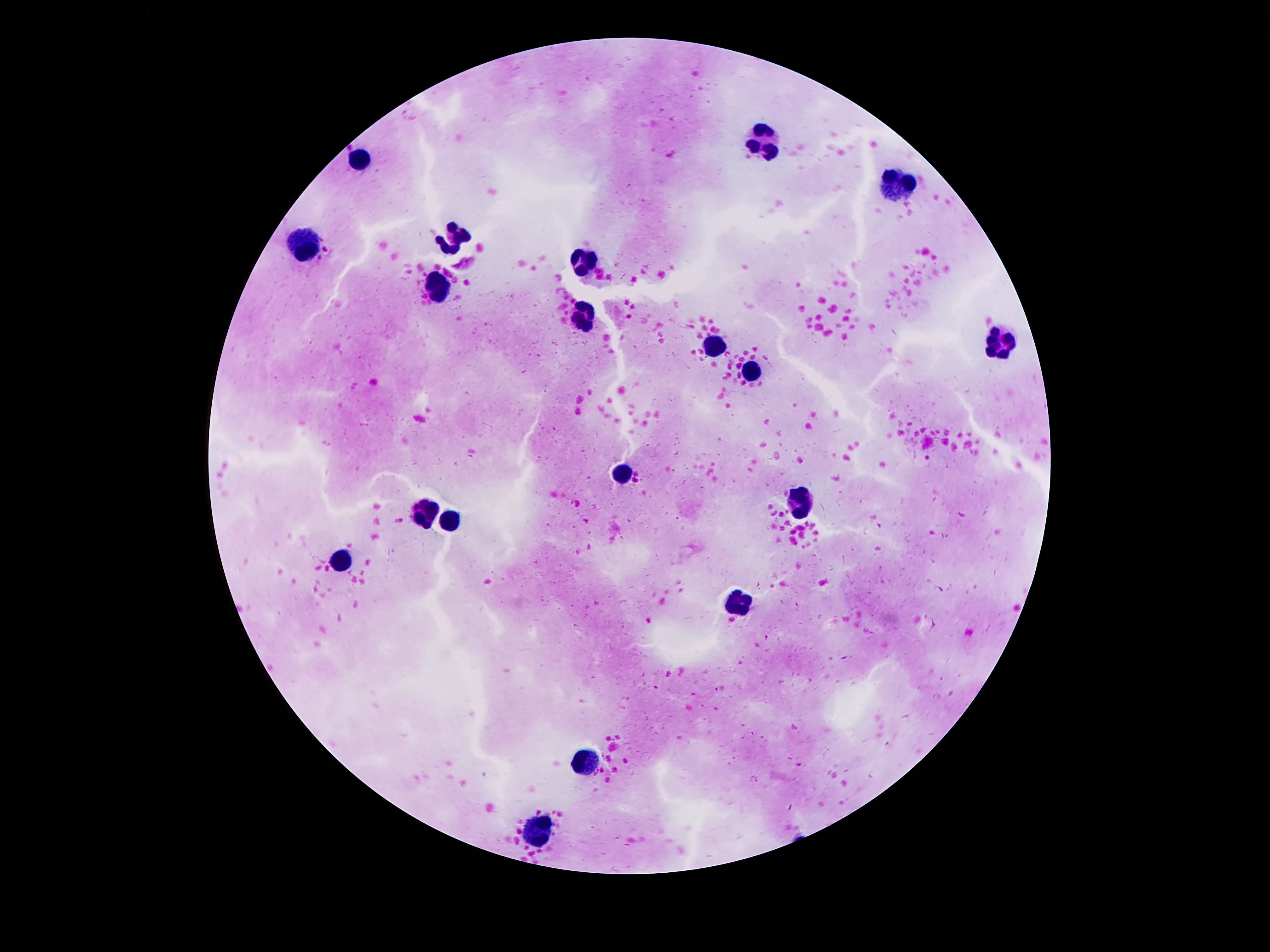

{
  "preparation": "thick blood smear",
  "image_size": "1270×952 pixels",
  "magnification": "100x",
  "patient_malaria_status": "uninfected",
  "capture": "smartphone camera through the microscope eyepiece",
  "field_of_view": "one from this slide",
  "leukocyte_locations": "approximate centers as [x, y] in pixels: [766, 141], [360, 159], [901, 186], [454, 235], [307, 243], [586, 261], [440, 285], [584, 317], [1002, 344], [715, 346], [752, 372], [625, 475], [803, 505], [424, 512], [448, 521], [344, 562], [741, 606], [590, 760], [543, 826]",
  "stain": "Giemsa"
}